Give the position of every malaria parasite.
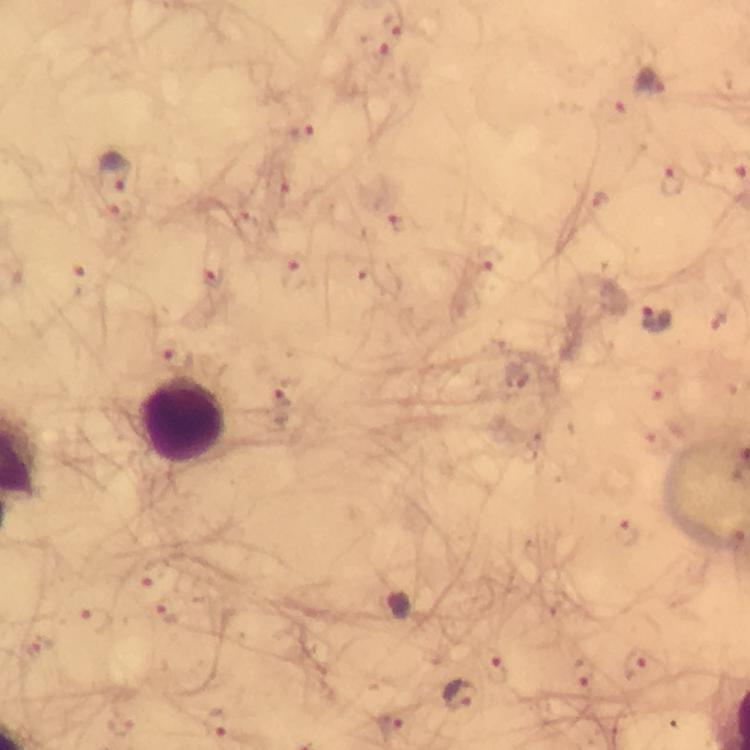

Approximate centers as [x, y] in pixels.
Malaria parasites: [393, 20], [373, 47], [650, 82], [612, 112], [300, 133], [115, 168], [673, 180], [281, 186], [600, 197], [116, 213], [404, 221], [487, 260], [297, 272], [85, 276], [212, 279], [657, 319], [178, 356], [665, 385], [284, 393], [651, 436], [628, 534], [154, 571], [166, 614], [97, 620], [36, 647], [637, 664], [584, 674], [497, 675], [460, 697], [394, 723], [123, 726], [216, 726].

Leukocyte locations: [184, 420]. Thick blood film. From a malaria diagnostic workup. Image is 750×750 pixels. At 100x magnification. Photographed through the microscope with a smartphone camera. Immersion oil applied. Giemsa-stained preparation. A crop from one field of view.